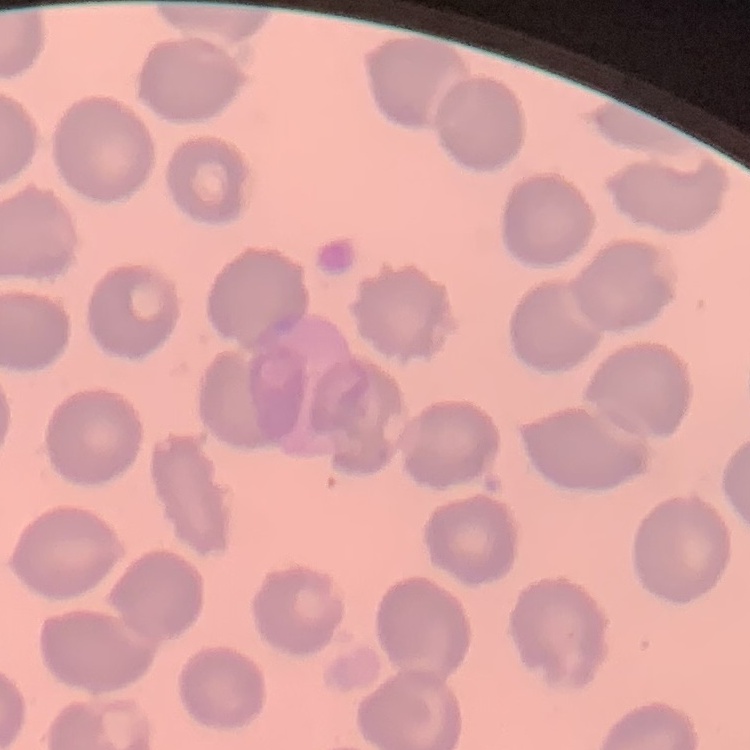

erythrocyte morphology = no rouleaux formation
stain = Field's or Giemsa
preparation = thin blood film
image type = square crop of a larger photomicrograph